Give the position of every Plasmodium parasite and every leukocyte.
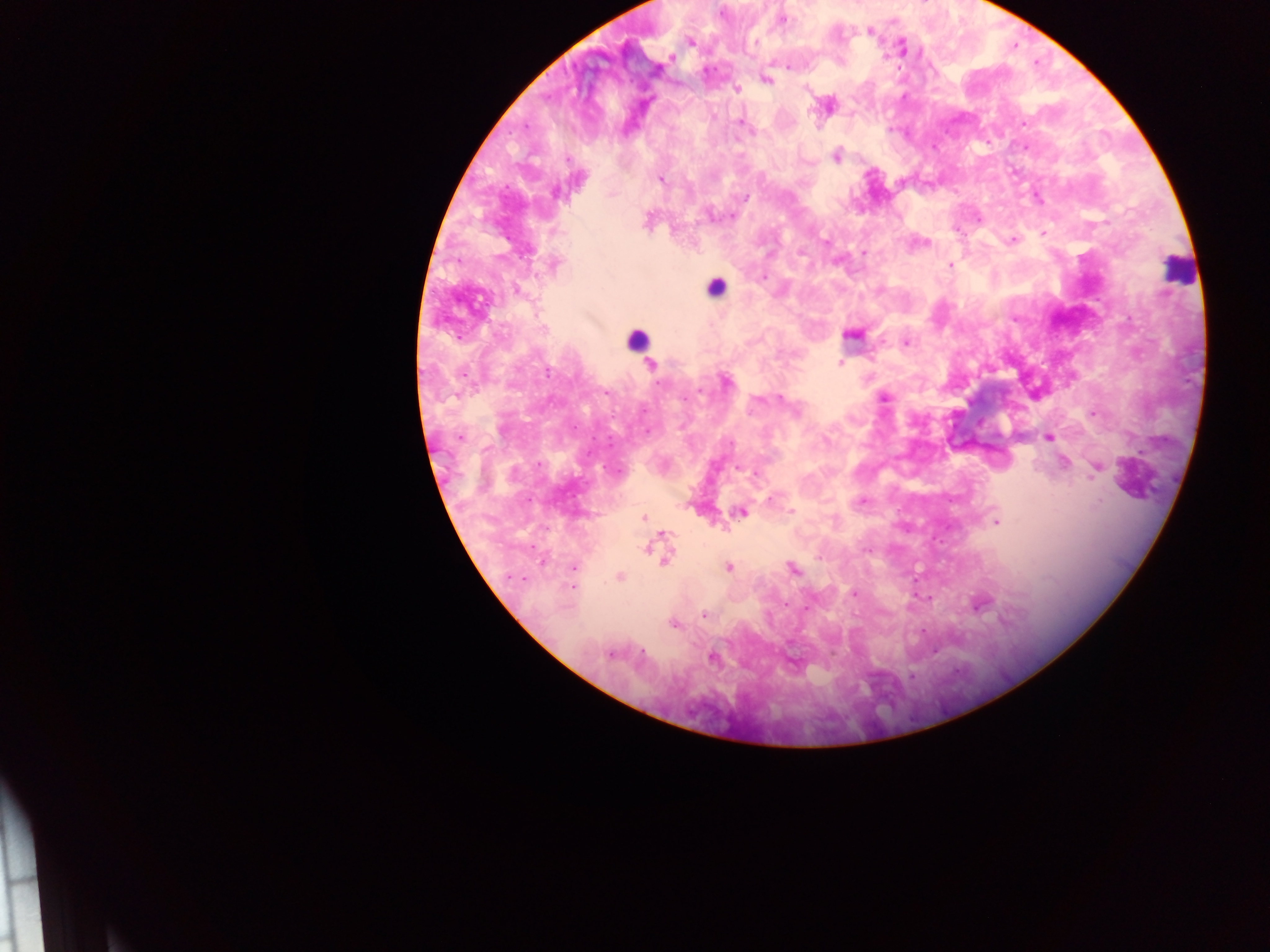
Approximate centers as x y in pixels.
Plasmodium parasites: 721 12; 781 20; 869 31; 690 42; 901 47; 671 57; 788 66; 765 79; 735 89; 826 105; 740 122; 836 155; 660 179; 1037 198; 731 215; 977 217; 1043 233; 1013 240; 923 242; 862 253; 553 264; 949 265; 517 290; 852 334; 906 343; 839 364; 649 366; 725 380; 883 397; 1092 413; 1048 436; 460 437; 1064 463; 1096 467; 771 498; 861 501; 742 511; 791 511; 644 517; 996 521; 662 538; 651 545; 866 551; 664 556; 573 566; 727 567; 791 568; 619 577; 572 586; 855 593; 929 598; 979 603; 702 613; 674 624; 611 653; 713 656; 911 676.
Leukocytes: 1178 269; 715 287; 635 339.

Summary:
  - Country: Ghana
  - Image size: 1270×952 pixels
  - Field of view: single
  - Capture: mobile-phone photograph through a microscope
  - Preparation: thick blood film